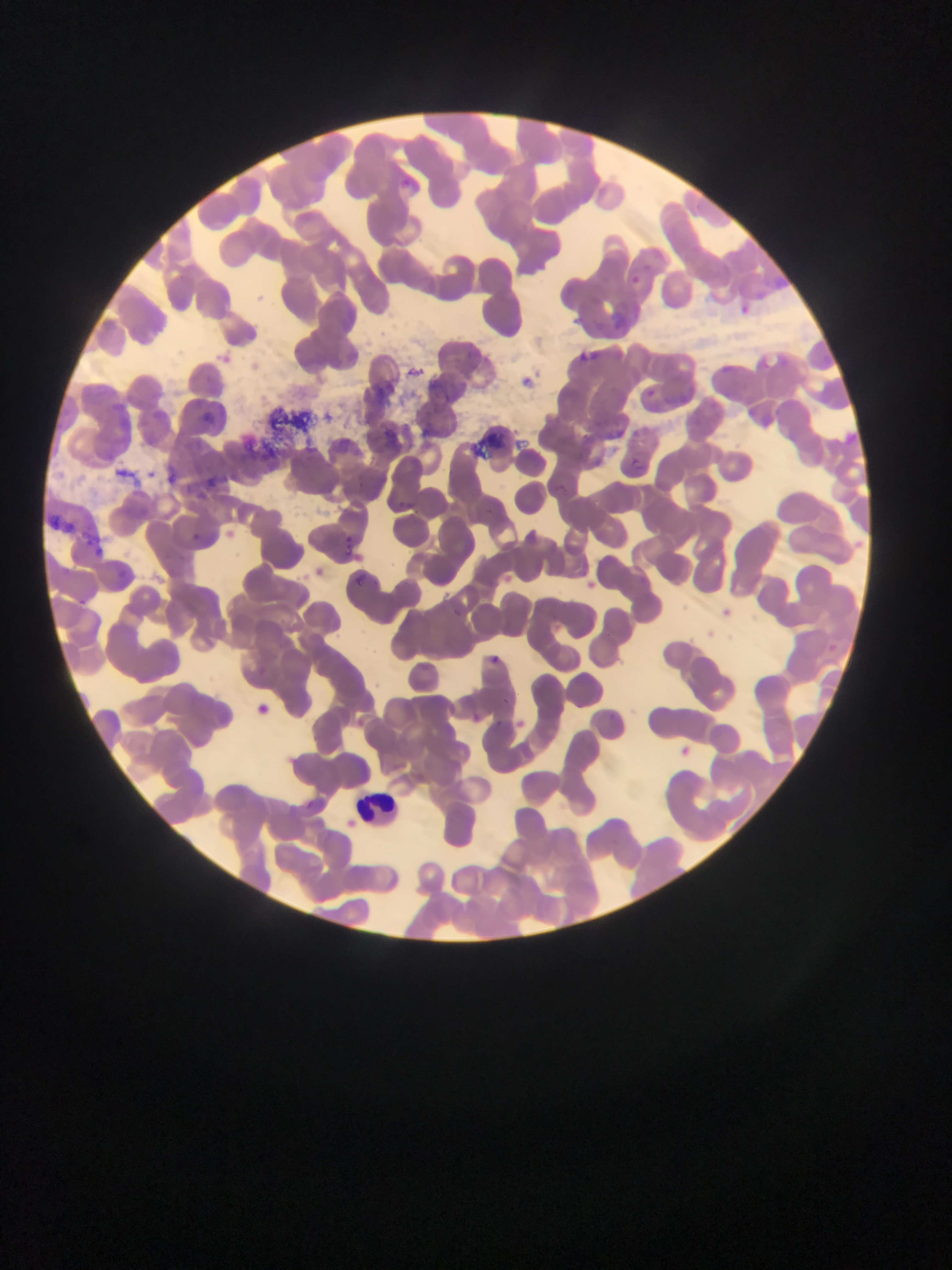

Approximate bounding boxes as (left, top, right, bottom) in pixels.
Summary:
  - Leukocyte locations: (346, 780, 402, 831)
  - Plasmodium parasite locations: (396, 171, 439, 202), (625, 270, 638, 288), (743, 296, 757, 324), (603, 310, 631, 328), (580, 346, 601, 364), (715, 359, 749, 390), (529, 363, 551, 396), (638, 380, 664, 408), (149, 384, 175, 435), (203, 401, 220, 420), (688, 405, 706, 440), (621, 453, 654, 481), (158, 459, 183, 485), (194, 467, 219, 489), (544, 478, 572, 496), (393, 492, 427, 513), (191, 526, 203, 543), (343, 534, 367, 559), (94, 549, 112, 565), (349, 566, 370, 588), (80, 599, 95, 612), (448, 599, 471, 624), (486, 646, 509, 669), (255, 660, 265, 676), (244, 698, 277, 721)
  - Country: Ghana
  - Capture: mobile-phone photograph through a microscope
  - Preparation: thin blood film
  - Image size: 952×1270 pixels
  - Field of view: single